Identify the cell.
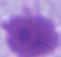
This is an erythrocyte.

Micrograph. Captured at 1000x magnification.